Give the extent of all Plasmodium falciparum-infected red blood cells.
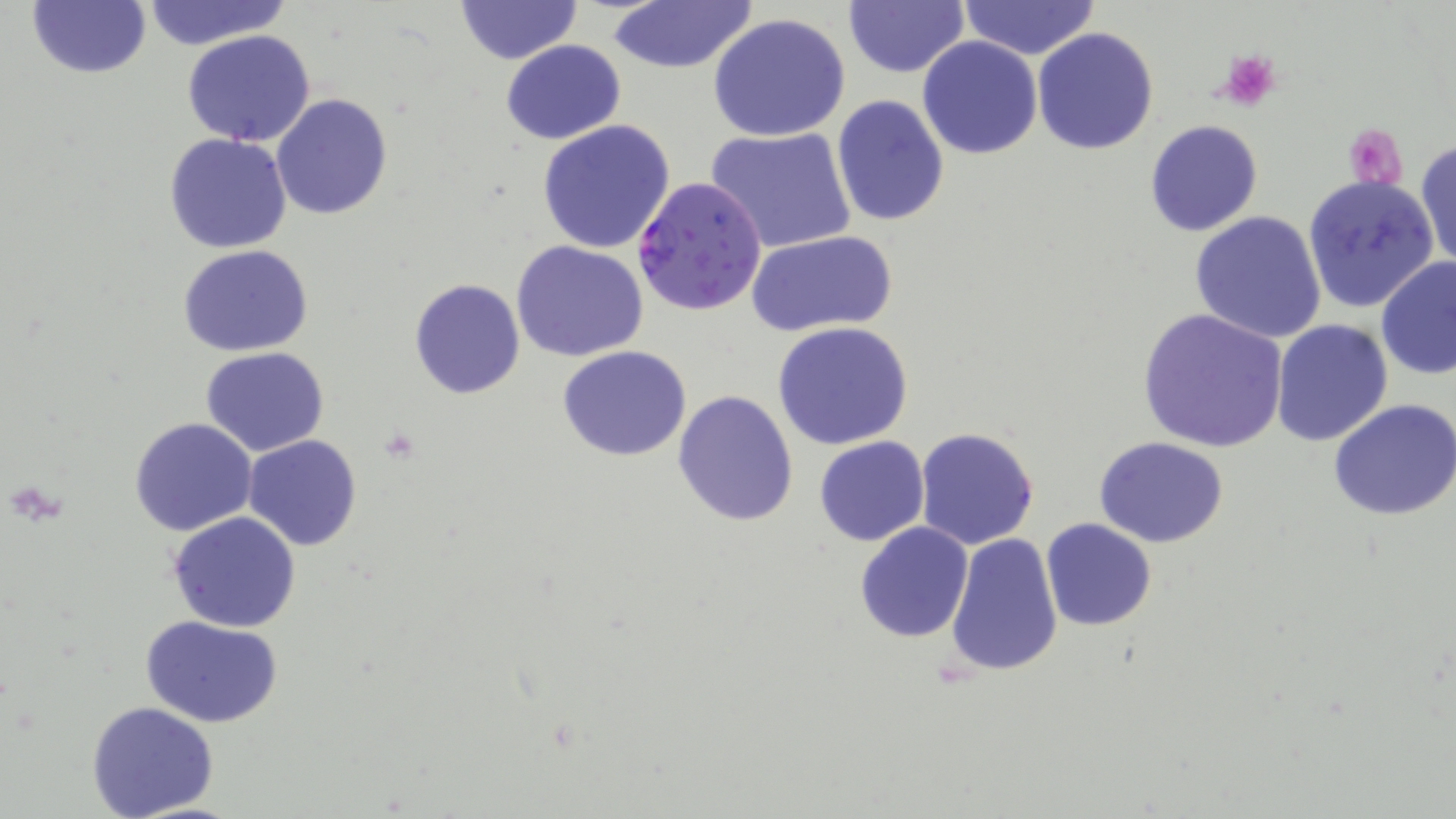

Approximate bounding boxes as named x1/y1/x2/y2 corners in pixels.
Plasmodium falciparum-infected red blood cells: (x1=633, y1=176, x2=766, y2=316).

slide-level diagnosis = Plasmodium falciparum
stain = May-Grünwald-Giemsa
platelet locations = approximate bounding boxes as named x1/y1/x2/y2 corners in pixels: (x1=1215, y1=49, x2=1283, y2=109), (x1=1344, y1=122, x2=1408, y2=191)
modality = light microscopy
image size = 1456×819 pixels
magnification = 1000x
preparation = thin blood film
uninfected red blood cell locations = approximate bounding boxes as named x1/y1/x2/y2 corners in pixels: (x1=25, y1=0, x2=152, y2=81), (x1=453, y1=0, x2=581, y2=64), (x1=843, y1=0, x2=968, y2=77), (x1=138, y1=1, x2=288, y2=51), (x1=609, y1=1, x2=755, y2=75), (x1=958, y1=1, x2=1099, y2=61), (x1=709, y1=13, x2=852, y2=141), (x1=1032, y1=26, x2=1159, y2=155), (x1=182, y1=29, x2=316, y2=147), (x1=917, y1=36, x2=1042, y2=159), (x1=501, y1=40, x2=625, y2=145), (x1=271, y1=94, x2=392, y2=221), (x1=830, y1=95, x2=951, y2=227), (x1=535, y1=118, x2=678, y2=253), (x1=1144, y1=120, x2=1264, y2=237), (x1=706, y1=126, x2=855, y2=254), (x1=164, y1=133, x2=293, y2=255), (x1=1416, y1=140, x2=1455, y2=268), (x1=1303, y1=174, x2=1440, y2=312), (x1=1190, y1=210, x2=1327, y2=344), (x1=747, y1=229, x2=898, y2=337), (x1=511, y1=239, x2=650, y2=362), (x1=177, y1=245, x2=314, y2=356), (x1=1376, y1=257, x2=1456, y2=379), (x1=409, y1=278, x2=526, y2=401), (x1=1137, y1=307, x2=1289, y2=452), (x1=1271, y1=319, x2=1394, y2=446), (x1=771, y1=321, x2=916, y2=450), (x1=558, y1=345, x2=692, y2=461), (x1=200, y1=346, x2=329, y2=456), (x1=672, y1=390, x2=799, y2=526), (x1=1329, y1=398, x2=1456, y2=520), (x1=130, y1=417, x2=257, y2=537), (x1=913, y1=427, x2=1041, y2=550), (x1=242, y1=434, x2=363, y2=550), (x1=813, y1=436, x2=929, y2=547), (x1=1094, y1=437, x2=1229, y2=548), (x1=168, y1=511, x2=302, y2=633), (x1=1041, y1=519, x2=1157, y2=632), (x1=854, y1=521, x2=974, y2=642), (x1=946, y1=531, x2=1064, y2=676), (x1=141, y1=615, x2=283, y2=727), (x1=86, y1=701, x2=220, y2=819)
field of view = single